State the preparation type.
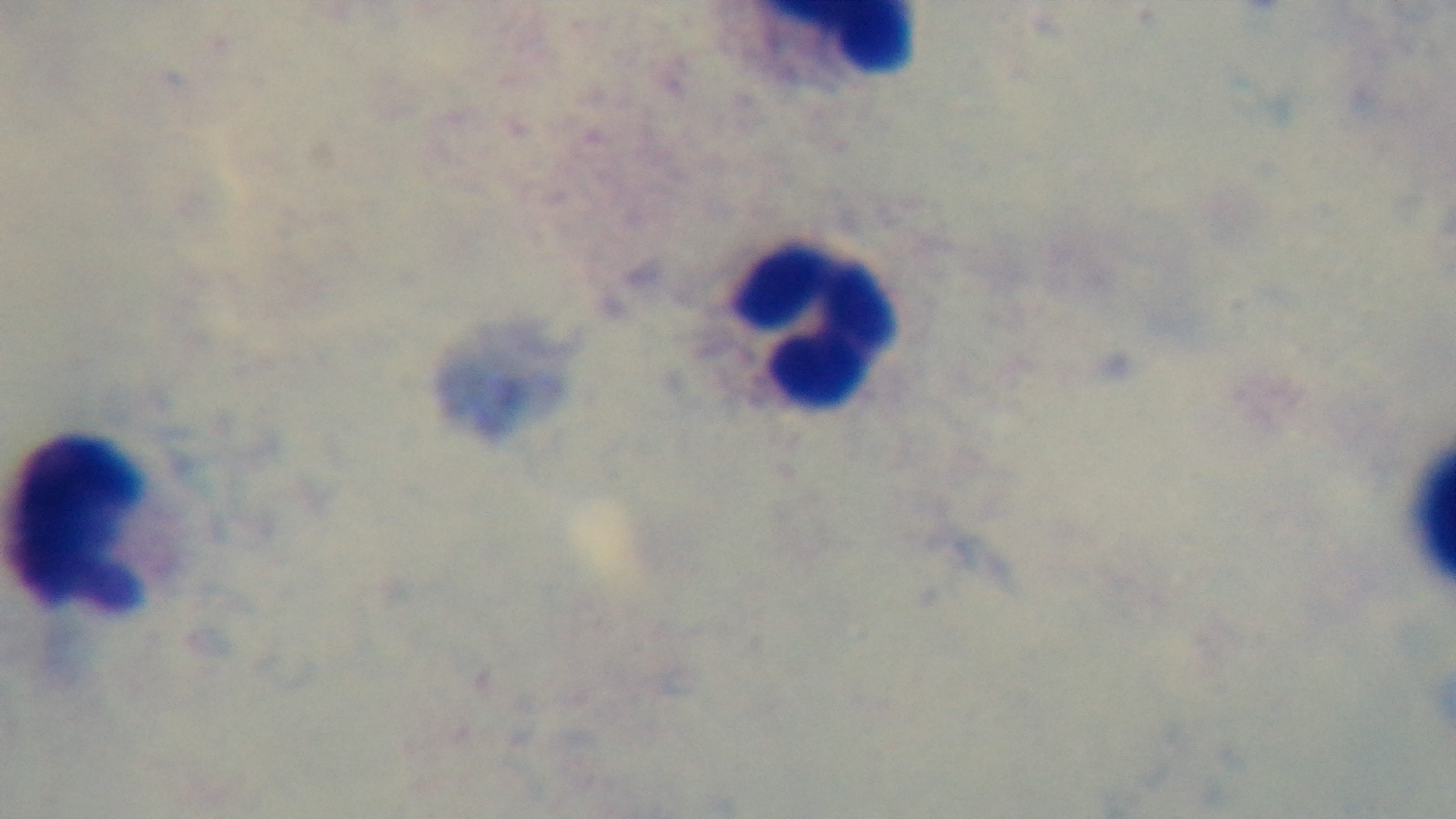
It is a thick blood film.

Oil-immersion objective, 100x. Single field of view. Light microscopy. Giemsa-stained. Malaria status: uninfected. Mounted 4K digital camera.